Report the malaria status of this cell.
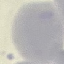
It is uninfected.

{
  "preparation": "thin blood smear",
  "image_type": "cell patch, automatically extracted from a larger field of view and resized to 64 × 64 pixels",
  "capture": "smartphone through the microscope eyepiece",
  "stain": "Giemsa"
}